Assess this cell for malaria.
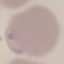
It is parasitized.

Giemsa-stained preparation. Cell patch, automatically extracted from a larger field of view and resized to 64 × 64 pixels. Thin smear of blood. Photographed with a smartphone camera at the microscope eyepiece.